Describe the morphology of the red blood cells.
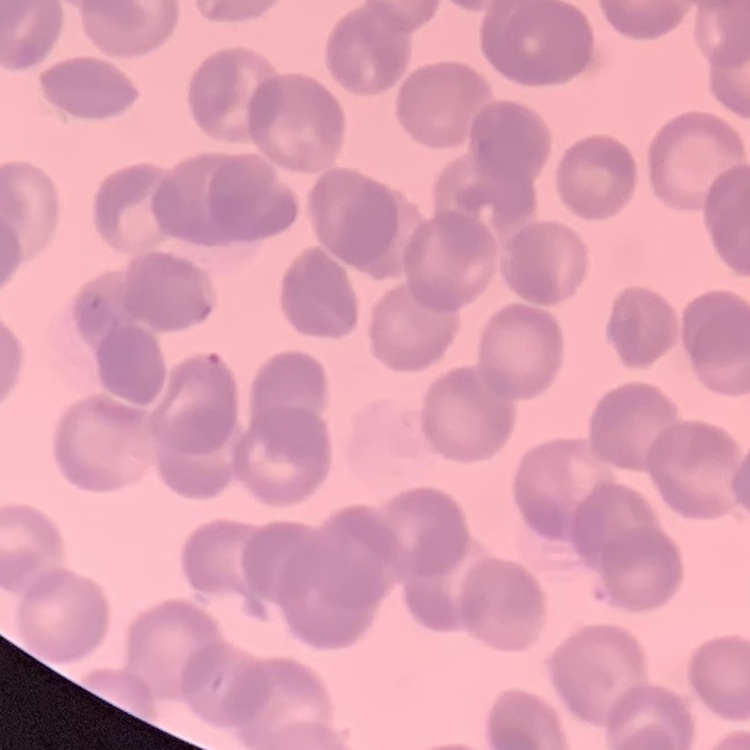
Rouleaux formation.

Thin blood smear. Stained with either Field's or Giemsa. One tile cut from a larger photomicrograph.